Comment on the morphology of the erythrocytes.
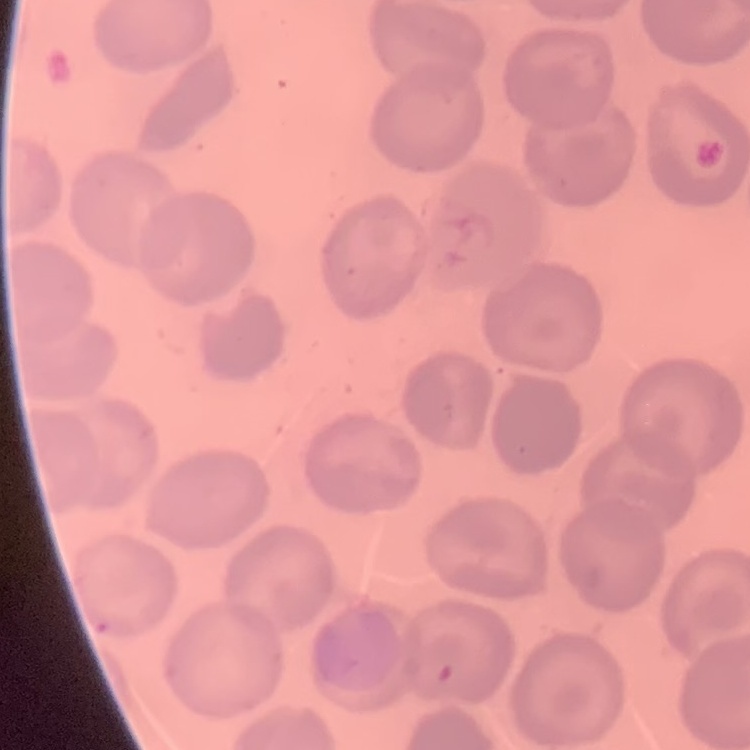
They show no rouleaux formation.

preparation = thin blood smear
stain = Field's or Giemsa
image type = square crop of a larger photomicrograph